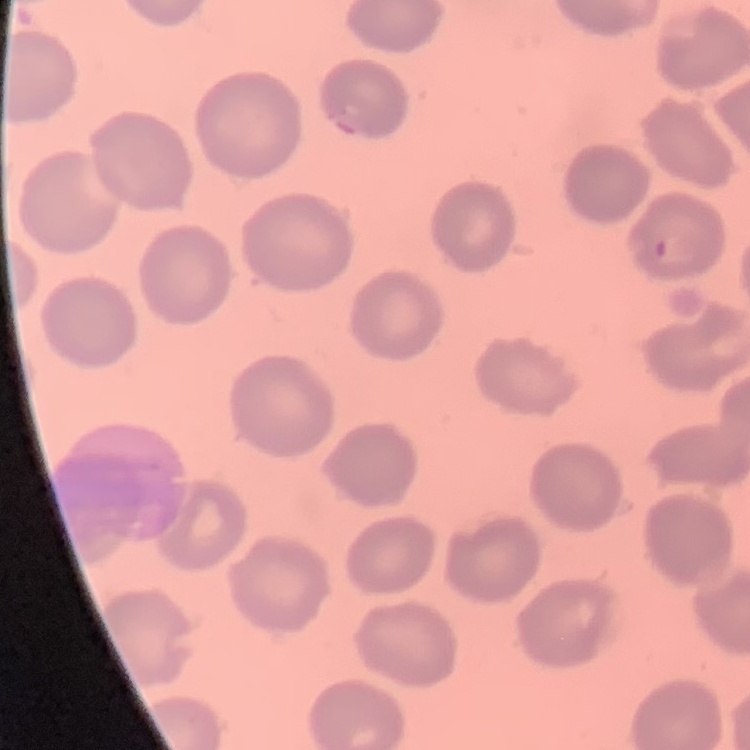

red blood cell morphology = no rouleaux formation
image type = one tile cut from a larger photomicrograph
preparation = thin blood smear
stain = Field's or Giemsa